State which cell type is depicted.
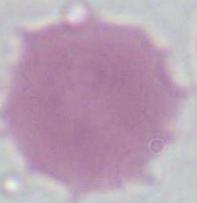

This is an erythrocyte.

Summary:
  - Modality: micrograph
  - Magnification: 1000x